Classify this cell by malaria status.
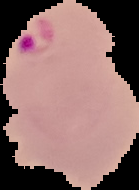
Parasitized.

image_type: segmented cell region with the area outside set to black
preparation: thin blood film
image_size: 139×190 pixels